Identify the blood parasite species.
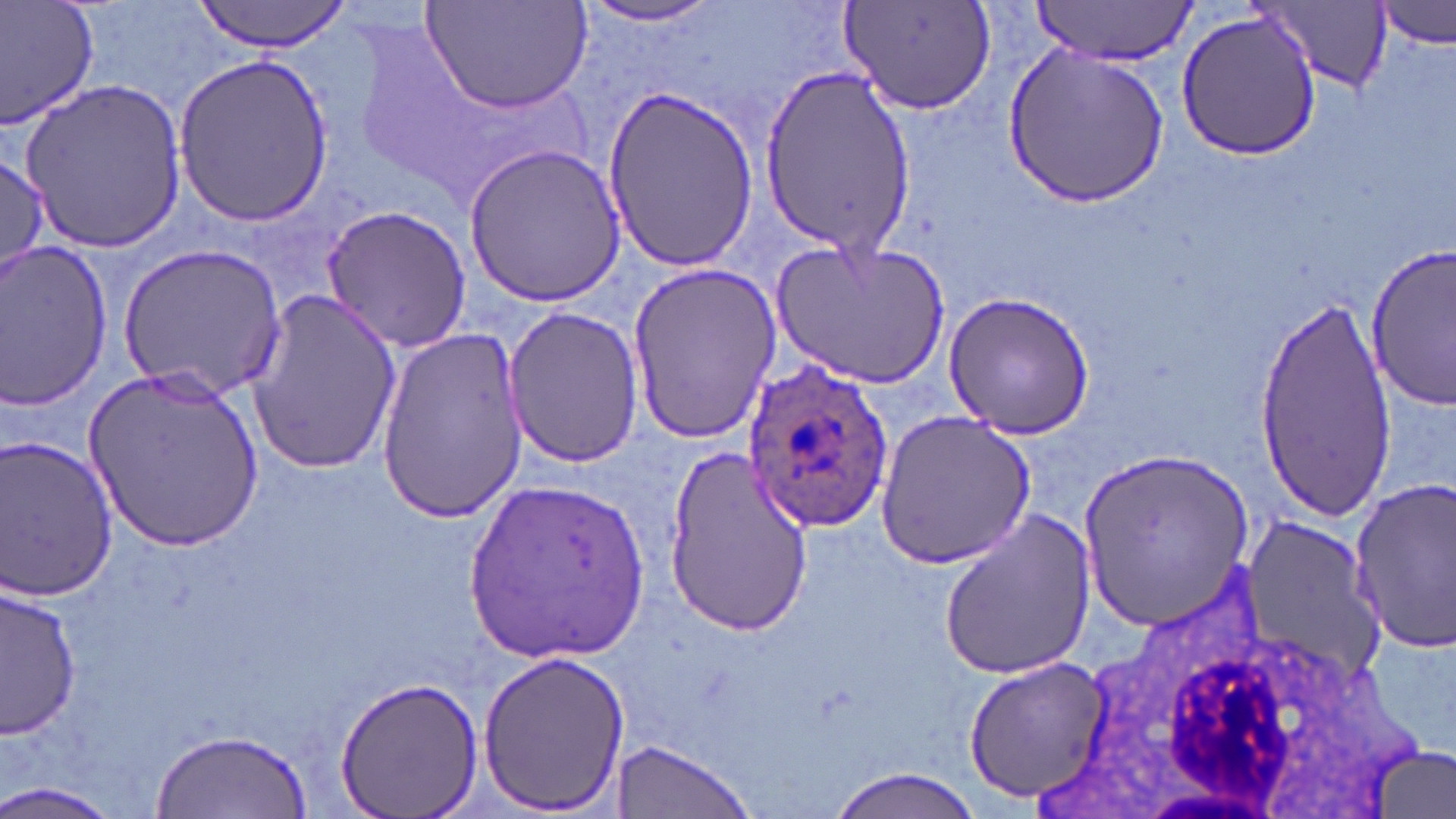

Plasmodium ovale.

Approximate bounding boxes as named x1/y1/x2/y2 corners in pixels. Uninfected red blood cell locations: (x1=1, y1=0, x2=101, y2=131), (x1=190, y1=0, x2=351, y2=53), (x1=421, y1=0, x2=593, y2=118), (x1=1031, y1=0, x2=1199, y2=66), (x1=1378, y1=0, x2=1454, y2=51), (x1=574, y1=1, x2=730, y2=30), (x1=1257, y1=1, x2=1393, y2=96), (x1=840, y1=2, x2=996, y2=115), (x1=1174, y1=6, x2=1322, y2=160), (x1=1003, y1=44, x2=1170, y2=205), (x1=173, y1=53, x2=337, y2=227), (x1=753, y1=70, x2=920, y2=250), (x1=20, y1=81, x2=193, y2=252), (x1=599, y1=90, x2=766, y2=269), (x1=464, y1=143, x2=627, y2=308), (x1=0, y1=154, x2=50, y2=278), (x1=320, y1=202, x2=472, y2=353), (x1=771, y1=238, x2=949, y2=388), (x1=1365, y1=242, x2=1454, y2=412), (x1=0, y1=243, x2=115, y2=409), (x1=121, y1=244, x2=287, y2=399), (x1=624, y1=263, x2=781, y2=446), (x1=942, y1=290, x2=1096, y2=439), (x1=242, y1=291, x2=403, y2=475), (x1=1251, y1=291, x2=1394, y2=518), (x1=503, y1=306, x2=644, y2=467), (x1=374, y1=327, x2=526, y2=522), (x1=86, y1=366, x2=263, y2=553), (x1=875, y1=410, x2=1035, y2=566), (x1=0, y1=436, x2=120, y2=603), (x1=662, y1=443, x2=815, y2=634), (x1=1081, y1=447, x2=1254, y2=636), (x1=1349, y1=473, x2=1455, y2=658), (x1=465, y1=475, x2=652, y2=662), (x1=936, y1=511, x2=1095, y2=683), (x1=1237, y1=517, x2=1388, y2=688), (x1=0, y1=584, x2=81, y2=739), (x1=475, y1=647, x2=631, y2=815), (x1=964, y1=656, x2=1107, y2=802), (x1=335, y1=672, x2=486, y2=819), (x1=152, y1=727, x2=311, y2=816), (x1=609, y1=741, x2=756, y2=818), (x1=1370, y1=744, x2=1455, y2=819), (x1=822, y1=769, x2=990, y2=819), (x1=0, y1=779, x2=122, y2=819). Plasmodium ovale-infected red blood cell locations: (x1=744, y1=363, x2=891, y2=535). White blood cell locations: (x1=1024, y1=557, x2=1430, y2=816). Light microscopy. Image is 1456×819 pixels. Thin blood film. One field of a larger specimen. May-Grünwald-Giemsa stain. 1000x magnification.